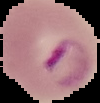

{
  "preparation": "thin blood film",
  "image_type": "cell region segmented out of the field of view; surrounding area masked to black",
  "image_size": "100×103 pixels",
  "result": "malaria parasites identified"
}